Assess the morphology of the erythrocytes.
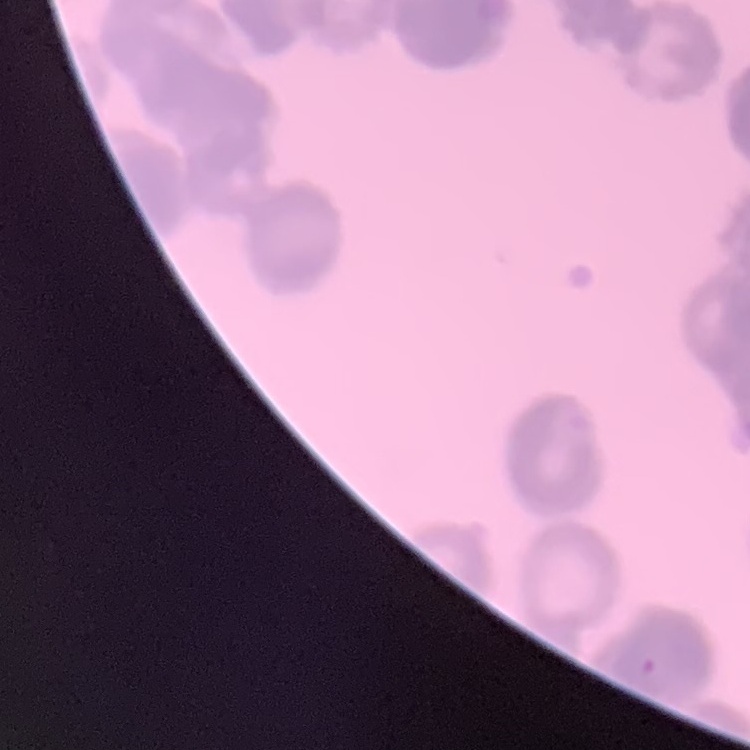

They show rouleaux formation.

Field's or Giemsa stain. Square crop of a larger photomicrograph. Thin peripheral smear.